Identify the preparation type.
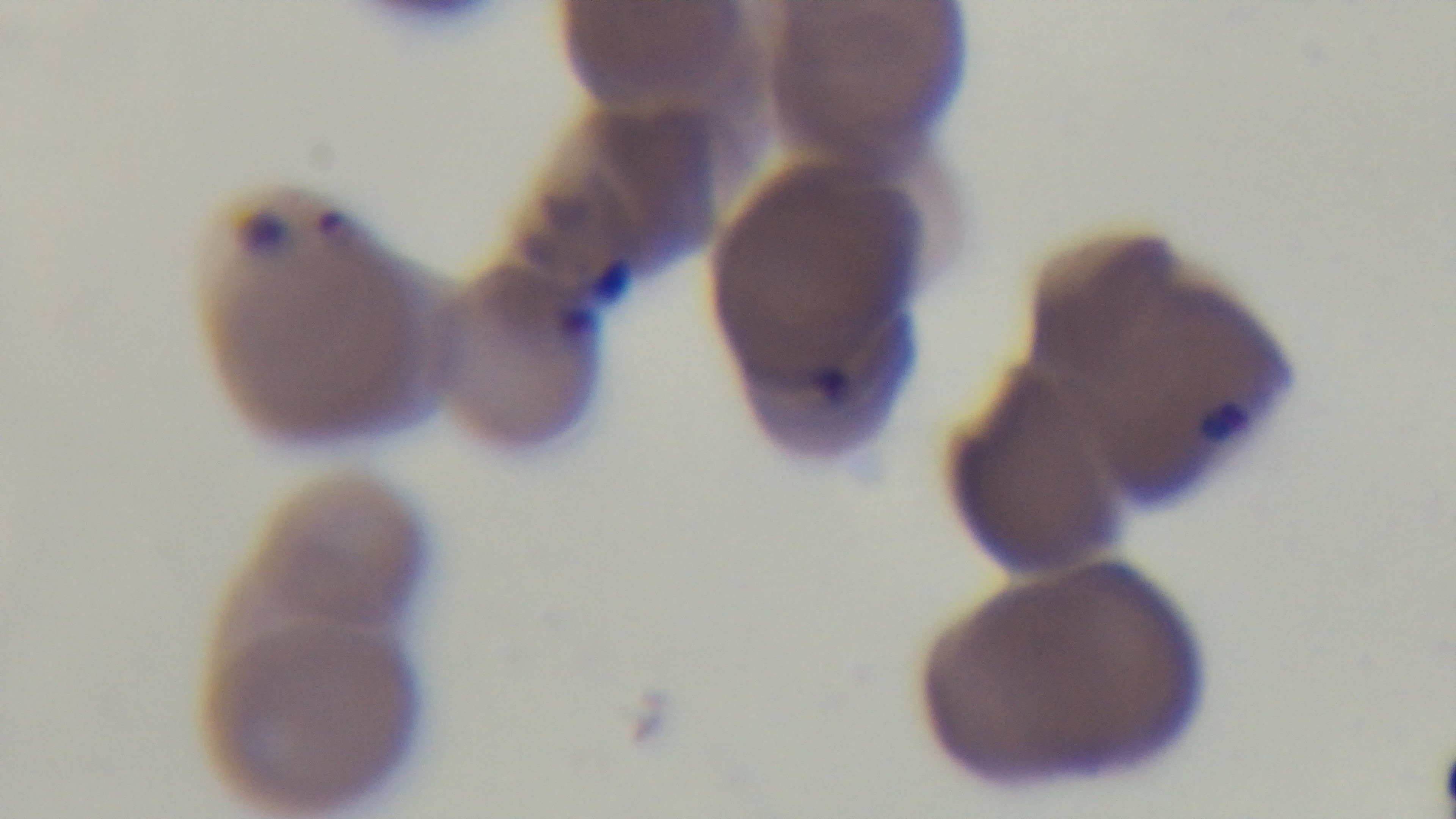

Thin.

field of view = single
malaria status = positive
stain = Giemsa
capture = mounted 4K digital camera
modality = light microscopy
objective = 100x oil immersion